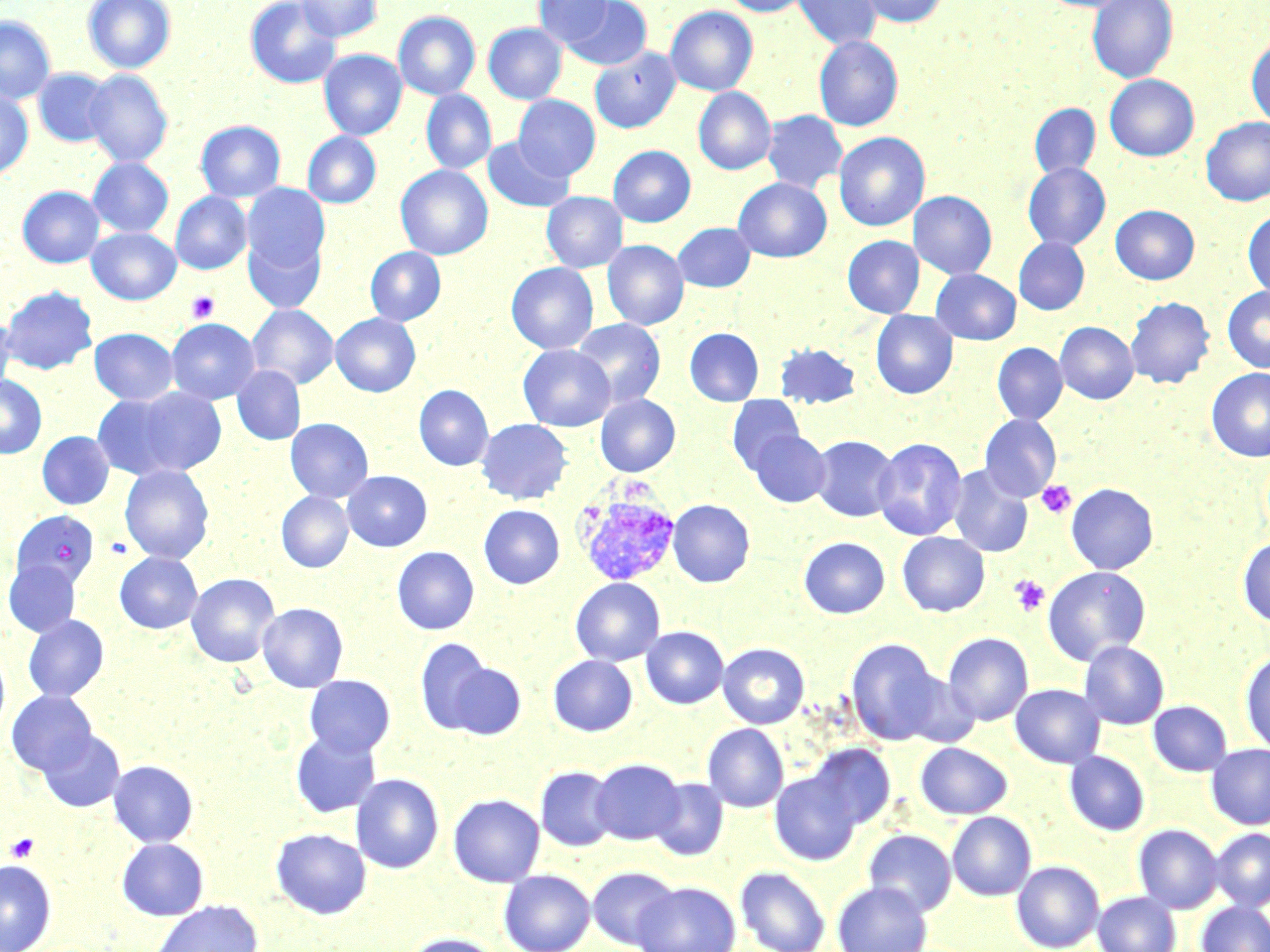 Approximate bounding boxes as [x1, y1, x2, y2] in pixels. Platelet locations: [187, 291, 220, 322], [1037, 480, 1076, 519], [1010, 575, 1050, 616], [5, 832, 40, 863]. Plasmodium vivax-infected red blood cell locations: [574, 487, 681, 587]. Uninfected red blood cell locations: [83, 0, 176, 74], [245, 0, 341, 89], [296, 0, 381, 42], [534, 0, 614, 48], [720, 0, 810, 17], [793, 0, 882, 50], [856, 0, 949, 27], [1088, 0, 1178, 83], [561, 1, 652, 71], [665, 6, 758, 97], [393, 11, 480, 100], [0, 16, 56, 105], [483, 23, 566, 104], [1246, 34, 1270, 129], [813, 35, 904, 131], [589, 47, 680, 134], [319, 49, 407, 140], [33, 68, 115, 148], [84, 70, 173, 167], [1105, 74, 1199, 161], [693, 87, 776, 175], [0, 89, 33, 180], [421, 89, 496, 175], [514, 95, 600, 181], [1029, 103, 1100, 179], [761, 110, 848, 193], [1200, 117, 1270, 206], [196, 120, 286, 202], [302, 132, 381, 209], [834, 132, 930, 231], [482, 137, 575, 212], [608, 146, 696, 227], [88, 157, 174, 237], [1023, 162, 1111, 251], [395, 165, 493, 260], [733, 177, 832, 263], [242, 183, 329, 275], [17, 186, 104, 268], [541, 191, 627, 273], [909, 191, 996, 279], [170, 192, 252, 275], [1110, 205, 1199, 284], [1243, 209, 1270, 299], [673, 223, 756, 292], [87, 227, 180, 304], [243, 230, 327, 313], [843, 235, 924, 318], [1013, 237, 1090, 315], [602, 240, 689, 331], [366, 247, 445, 325], [506, 262, 599, 354], [931, 269, 1021, 345], [2, 285, 98, 374], [1222, 285, 1270, 373], [1125, 296, 1215, 389], [247, 305, 338, 390], [870, 310, 958, 399], [331, 313, 420, 397], [0, 316, 16, 397], [167, 318, 260, 404], [572, 319, 666, 407], [1055, 322, 1138, 404], [90, 328, 179, 405], [685, 328, 764, 405], [775, 342, 860, 408], [992, 342, 1068, 425], [518, 344, 615, 431], [232, 365, 305, 445], [1206, 368, 1270, 462], [0, 374, 47, 458], [414, 385, 493, 471], [123, 387, 229, 476], [91, 392, 190, 480], [595, 394, 680, 476], [726, 395, 806, 476], [979, 414, 1061, 502], [285, 418, 373, 503], [476, 418, 573, 504], [748, 430, 831, 507], [36, 431, 114, 510], [811, 435, 899, 522], [872, 437, 967, 541], [947, 463, 1034, 558], [119, 464, 214, 564], [343, 470, 431, 551], [1066, 483, 1158, 574], [276, 491, 353, 573], [667, 499, 754, 588], [479, 504, 564, 589], [10, 512, 100, 595], [897, 532, 990, 616], [1238, 536, 1270, 626], [799, 537, 890, 618], [392, 546, 479, 635], [114, 552, 202, 633], [4, 560, 82, 637], [1042, 565, 1151, 665], [186, 573, 280, 667], [570, 578, 665, 666], [257, 602, 348, 692], [23, 614, 109, 702], [641, 627, 728, 709], [943, 632, 1033, 726], [413, 638, 499, 735], [846, 638, 943, 745], [1078, 641, 1169, 729], [718, 643, 809, 728], [0, 645, 10, 740], [1240, 650, 1270, 754], [549, 655, 638, 736], [441, 658, 526, 739], [304, 674, 395, 757], [1010, 684, 1105, 768], [6, 690, 97, 777], [1148, 700, 1233, 776], [702, 723, 788, 812], [37, 729, 125, 813], [290, 730, 382, 818], [915, 742, 1012, 818], [806, 744, 895, 831], [1206, 744, 1270, 829], [1064, 751, 1149, 835], [591, 758, 684, 844], [108, 760, 198, 847], [536, 766, 618, 851], [770, 770, 862, 865], [351, 773, 444, 874], [649, 777, 728, 861], [448, 793, 544, 887], [947, 811, 1036, 900], [1133, 824, 1224, 913], [271, 827, 372, 919], [1211, 828, 1270, 910], [863, 829, 956, 916], [117, 837, 209, 920], [0, 860, 56, 952], [1011, 860, 1104, 951], [587, 866, 679, 949], [736, 866, 830, 952], [499, 869, 595, 952], [633, 881, 740, 952], [833, 881, 932, 952], [1093, 891, 1181, 952], [151, 900, 263, 952], [1196, 901, 1270, 952], [403, 933, 503, 952]. Slide-level diagnosis: Plasmodium vivax. 1000x magnification. May-Grünwald-Giemsa stain. Image is 1270×952 pixels. Thin blood film. Single field of view. Light microscopy.